Assess this cell for malaria.
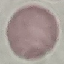
Uninfected.

image type = automatically extracted cell patch, resized to 64 × 64 pixels
preparation = thin blood smear
capture = smartphone through the microscope eyepiece
stain = Giemsa